State which parasite is depicted.
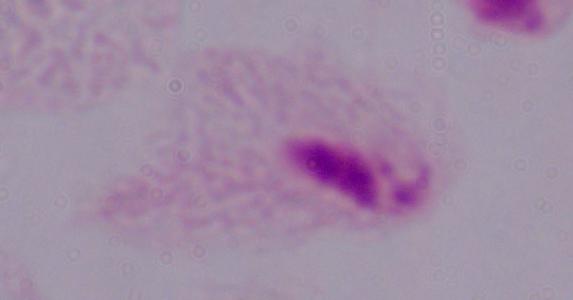
A trichomonad.

{
  "modality": "micrograph",
  "magnification": "1000x"
}